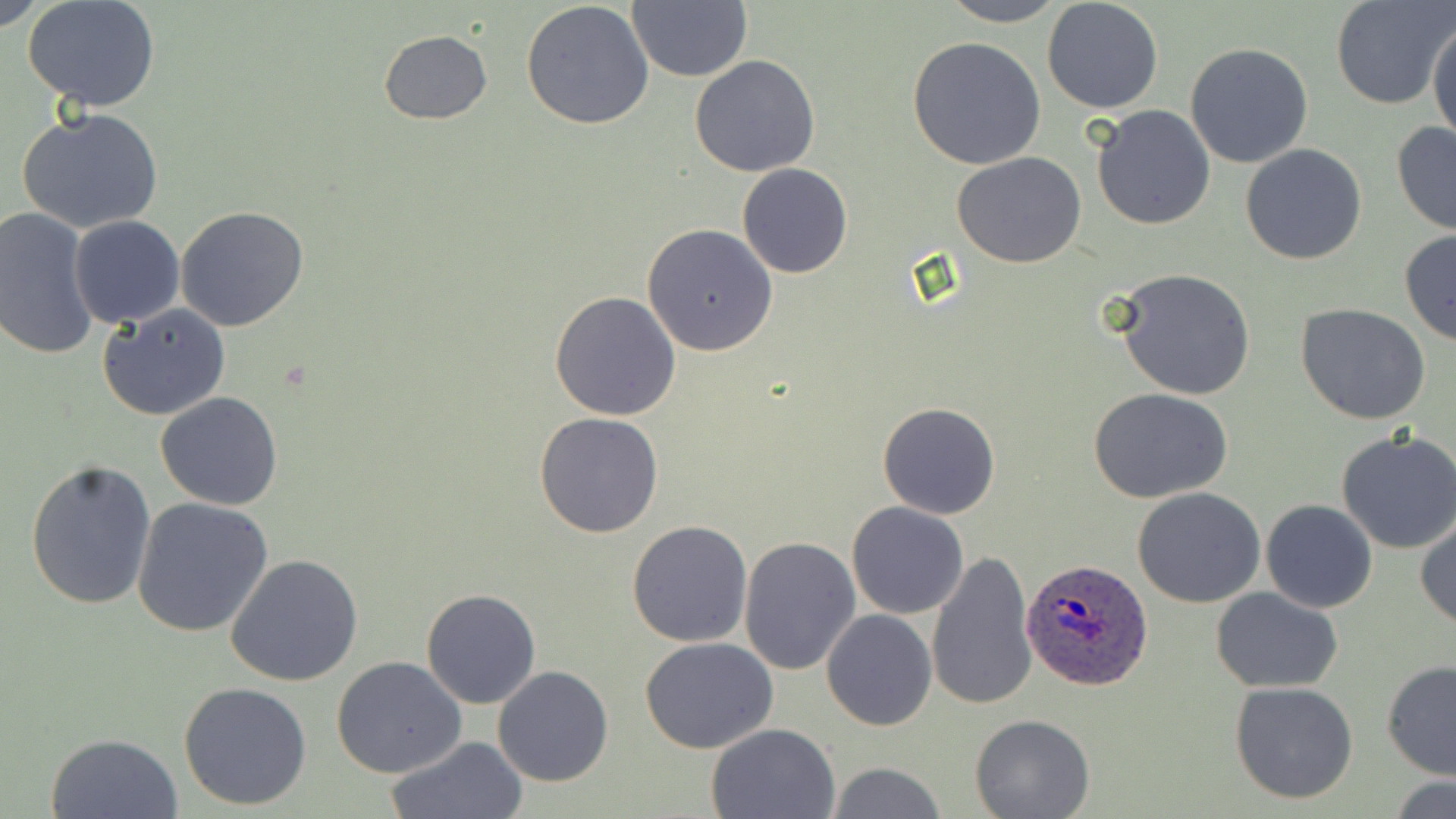

Summary:
  - Coordinate format: approximate bounding boxes as named x1/y1/x2/y2 corners in pixels
  - Plasmodium ovale-infected red blood cell locations: (x1=1022, y1=557, x2=1151, y2=690)
  - Uninfected red blood cell locations: (x1=0, y1=0, x2=50, y2=30), (x1=626, y1=0, x2=750, y2=84), (x1=935, y1=0, x2=1069, y2=26), (x1=1042, y1=0, x2=1164, y2=115), (x1=1328, y1=0, x2=1452, y2=111), (x1=23, y1=1, x2=162, y2=112), (x1=520, y1=2, x2=654, y2=133), (x1=1427, y1=19, x2=1455, y2=147), (x1=378, y1=30, x2=492, y2=124), (x1=907, y1=38, x2=1046, y2=171), (x1=1185, y1=43, x2=1314, y2=168), (x1=690, y1=54, x2=821, y2=177), (x1=1092, y1=105, x2=1215, y2=230), (x1=16, y1=107, x2=164, y2=234), (x1=1390, y1=121, x2=1456, y2=235), (x1=1240, y1=143, x2=1368, y2=265), (x1=952, y1=151, x2=1086, y2=268), (x1=737, y1=163, x2=852, y2=279), (x1=175, y1=206, x2=308, y2=332), (x1=1, y1=207, x2=99, y2=361), (x1=69, y1=215, x2=186, y2=327), (x1=643, y1=223, x2=780, y2=357), (x1=1399, y1=230, x2=1456, y2=346), (x1=1111, y1=268, x2=1256, y2=401), (x1=549, y1=291, x2=681, y2=421), (x1=99, y1=303, x2=231, y2=420), (x1=1297, y1=304, x2=1432, y2=425), (x1=1088, y1=387, x2=1234, y2=503), (x1=156, y1=391, x2=283, y2=511), (x1=878, y1=401, x2=1000, y2=519), (x1=534, y1=412, x2=664, y2=538), (x1=1335, y1=430, x2=1456, y2=555), (x1=25, y1=458, x2=156, y2=611), (x1=1132, y1=487, x2=1266, y2=608), (x1=132, y1=497, x2=274, y2=637), (x1=1261, y1=499, x2=1378, y2=614), (x1=846, y1=501, x2=970, y2=619), (x1=1415, y1=517, x2=1456, y2=630), (x1=626, y1=520, x2=753, y2=648), (x1=738, y1=533, x2=861, y2=675), (x1=926, y1=549, x2=1037, y2=713), (x1=224, y1=554, x2=365, y2=687), (x1=1211, y1=587, x2=1345, y2=693), (x1=421, y1=589, x2=541, y2=709), (x1=822, y1=609, x2=937, y2=731), (x1=640, y1=638, x2=779, y2=754), (x1=332, y1=656, x2=466, y2=778), (x1=1381, y1=660, x2=1456, y2=780), (x1=492, y1=666, x2=614, y2=786), (x1=1229, y1=680, x2=1359, y2=804), (x1=178, y1=681, x2=313, y2=811), (x1=970, y1=714, x2=1094, y2=819), (x1=706, y1=722, x2=843, y2=818), (x1=44, y1=731, x2=184, y2=819), (x1=387, y1=737, x2=527, y2=818), (x1=826, y1=762, x2=947, y2=818), (x1=1386, y1=776, x2=1456, y2=817)
  - Slide-level diagnosis: Plasmodium ovale
  - Image size: 1456×819 pixels
  - Magnification: 1000x
  - Field of view: single
  - Modality: light microscopy
  - Stain: May-Grünwald-Giemsa
  - Preparation: thin blood smear